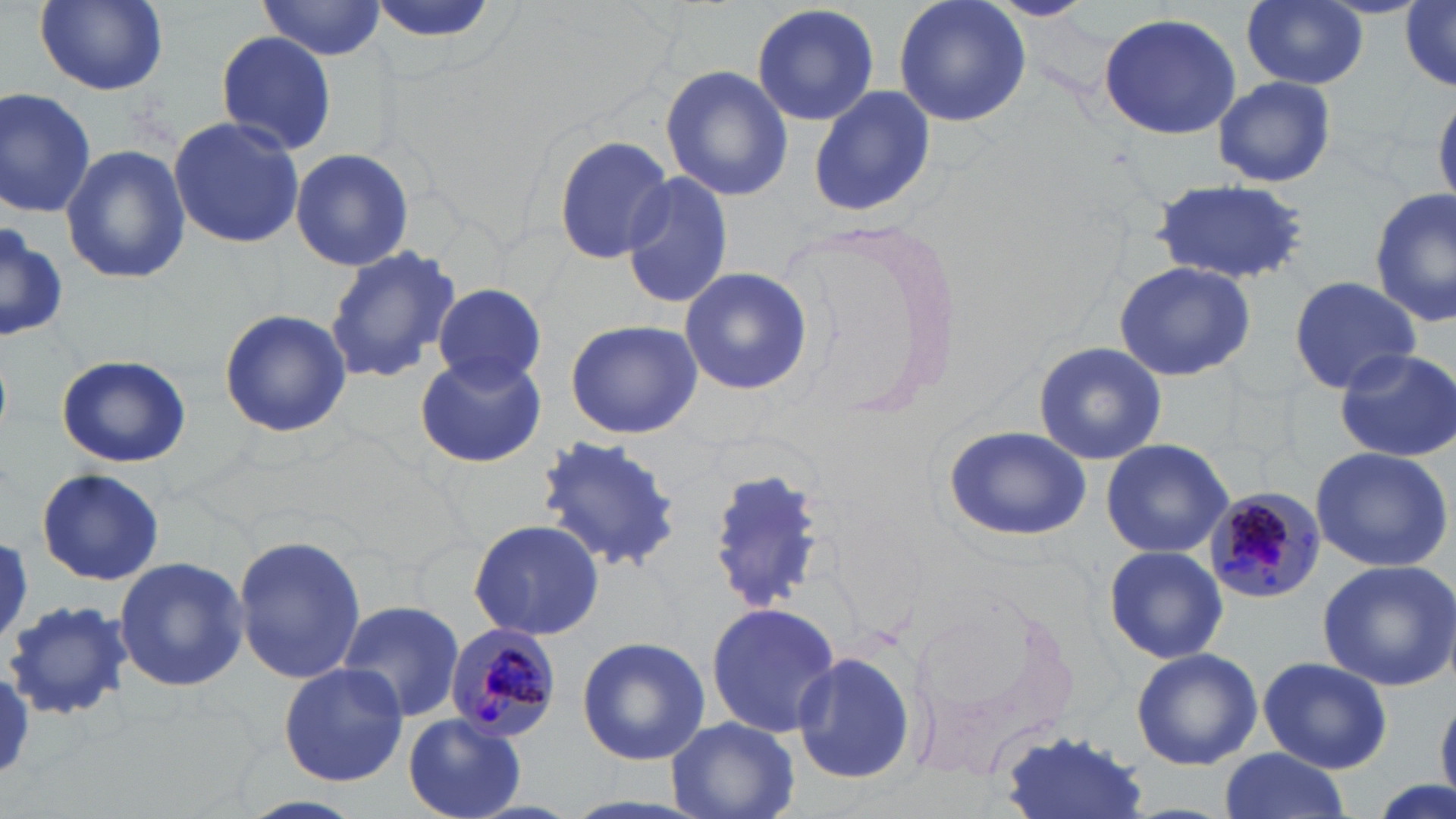

Summary:
  - Coordinate format: approximate bounding boxes as (x1,y1)-(x2,y2) corner pairs in pixels
  - Plasmodium malariae-infected red blood cell locations: (1203,486)-(1324,603), (442,623)-(564,747)
  - White blood cell locations: (9,600)-(130,725)
  - Uninfected red blood cell locations: (35,0)-(167,95), (892,0)-(1030,129), (985,0)-(1097,22), (1242,0)-(1369,89), (257,1)-(388,61), (1402,2)-(1456,89), (751,3)-(880,127), (1095,12)-(1242,140), (213,30)-(338,154), (660,63)-(794,200), (1213,75)-(1337,188), (807,84)-(937,220), (0,87)-(98,218), (1434,90)-(1456,210), (168,116)-(305,249), (553,132)-(672,262), (59,143)-(189,287), (290,148)-(415,273), (621,170)-(733,311), (1149,177)-(1310,287), (1371,188)-(1455,328), (0,220)-(67,346), (324,245)-(462,386), (1112,261)-(1257,383), (678,267)-(812,396), (1287,275)-(1422,394), (432,285)-(546,388), (218,309)-(352,438), (564,319)-(703,440), (1032,340)-(1167,465), (1333,346)-(1456,461), (413,350)-(548,469), (55,355)-(192,467), (938,423)-(1098,543), (533,433)-(686,577), (1100,437)-(1236,559), (1307,446)-(1453,573), (35,468)-(165,586), (706,468)-(830,618), (469,518)-(604,641), (232,533)-(366,687), (1102,544)-(1229,665), (112,557)-(249,691), (1317,560)-(1456,690), (899,593)-(1090,786), (333,599)-(465,722), (1,600)-(130,723), (704,601)-(843,738), (577,635)-(710,765), (1130,646)-(1263,771), (789,648)-(919,788), (1256,656)-(1392,773), (277,663)-(408,787), (405,713)-(526,818), (665,716)-(800,819), (998,727)-(1151,819), (1216,750)-(1351,818), (1372,776)-(1453,819)
  - Slide-level diagnosis: Plasmodium malariae
  - Modality: optical microscopy
  - Magnification: 1000x
  - Preparation: thin blood smear
  - Stain: May-Grünwald-Giemsa
  - Image size: 1456×819 pixels
  - Field of view: single